Locate leukocytes (white blood cells).
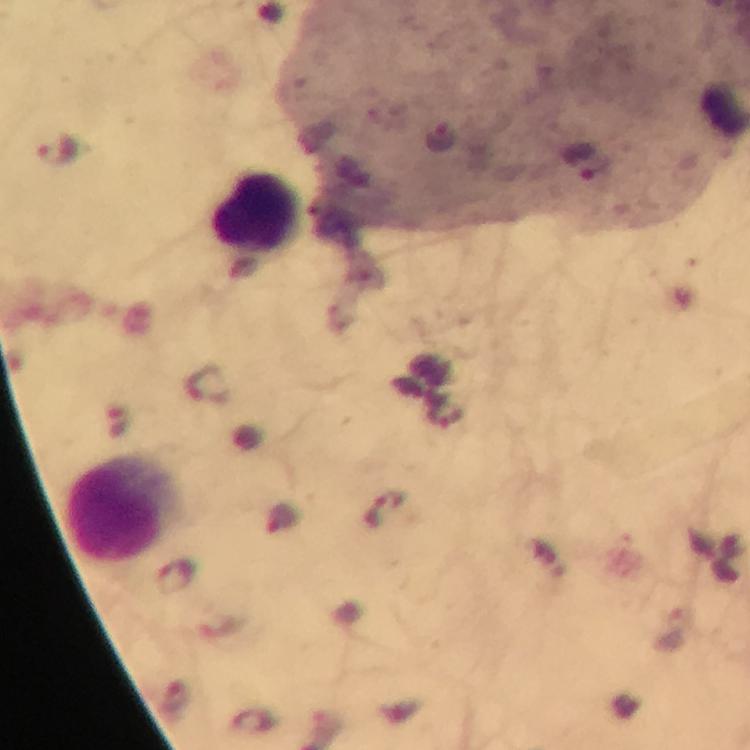

Approximate centers as (x, y) in pixels.
Leukocytes: (255, 213), (117, 510).

Summary:
  - Malaria parasite locations: (57, 149), (385, 509)
  - Preparation: thick blood smear
  - Image size: 750×750 pixels
  - Context: from a diagnostic examination for malaria
  - Capture: smartphone mounted on the microscope
  - Stain: Giemsa
  - Immersion oil: applied
  - Cropped from: a single field of view
  - Magnification: 100x